Classify this cell by malaria status.
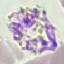

It is parasitized.

Giemsa-stained preparation. Thin blood smear. Automatically extracted cell patch, resized to 64 × 64 pixels. Photographed with a smartphone camera at the microscope eyepiece.